Assess the morphology of the red blood cells.
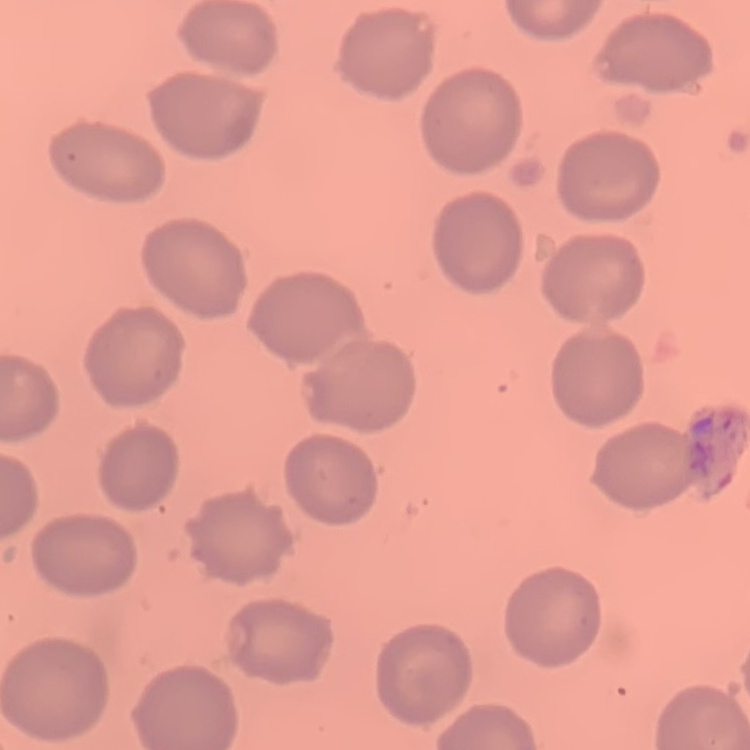
They show no rouleaux formation.

image_type: one tile cut from a larger photomicrograph
stain: Field's or Giemsa
preparation: thin blood smear